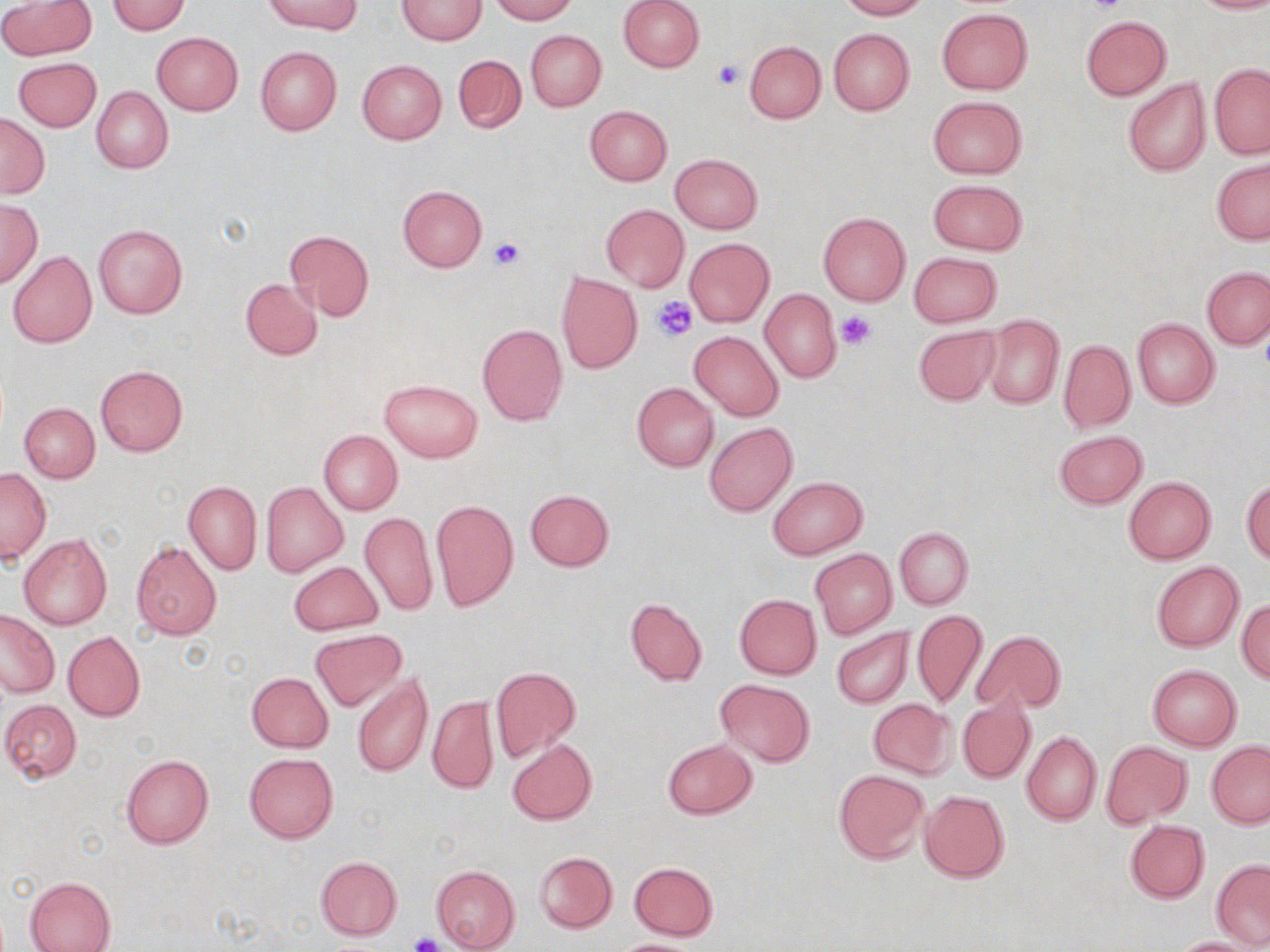

Approximate bounding boxes as (x1, y1, x2, y2) in pixels. Uninfected red blood cell locations: (266, 0, 361, 35), (489, 0, 578, 23), (617, 0, 705, 72), (837, 0, 929, 20), (1189, 0, 1270, 14), (1, 1, 95, 60), (105, 1, 191, 35), (397, 1, 486, 45), (937, 9, 1032, 94), (1080, 16, 1171, 100), (828, 28, 914, 116), (526, 30, 606, 111), (151, 31, 243, 116), (745, 40, 826, 122), (255, 46, 341, 135), (452, 54, 526, 133), (12, 57, 101, 131), (356, 59, 446, 143), (1209, 64, 1270, 159), (1123, 78, 1210, 178), (91, 87, 172, 174), (927, 95, 1026, 179), (584, 105, 672, 186), (0, 113, 50, 199), (670, 153, 762, 232), (1212, 158, 1269, 244), (927, 179, 1027, 255), (397, 184, 488, 272), (0, 199, 42, 286), (601, 204, 688, 291), (818, 212, 910, 305), (94, 224, 188, 319), (284, 227, 375, 321), (684, 237, 775, 328), (8, 251, 97, 348), (909, 252, 1002, 327), (1201, 267, 1270, 349), (555, 271, 643, 374), (240, 279, 322, 360), (760, 290, 840, 384), (984, 315, 1063, 409), (1132, 318, 1219, 408), (477, 323, 567, 425), (913, 324, 1000, 406), (689, 331, 784, 421), (1058, 339, 1135, 432), (95, 366, 188, 455), (381, 378, 482, 462), (632, 383, 718, 472), (19, 402, 99, 482), (705, 423, 796, 517), (1053, 430, 1148, 509), (319, 431, 401, 515), (0, 469, 51, 563), (768, 476, 867, 559), (1123, 476, 1216, 564), (1241, 479, 1270, 563), (184, 480, 261, 575), (262, 481, 347, 576), (525, 489, 615, 571), (430, 498, 519, 611), (360, 510, 438, 617), (895, 527, 972, 609), (19, 533, 112, 630), (131, 541, 221, 639), (810, 548, 897, 638), (289, 561, 383, 635), (1151, 561, 1243, 652), (734, 594, 821, 678), (625, 597, 707, 686), (1237, 599, 1270, 684), (0, 609, 59, 697), (911, 610, 987, 709), (831, 626, 913, 708), (311, 629, 403, 710), (972, 629, 1063, 716), (63, 630, 146, 721), (1148, 664, 1241, 750), (490, 666, 581, 762), (246, 672, 332, 752), (352, 673, 431, 778), (716, 679, 814, 766), (957, 692, 1036, 785), (427, 695, 497, 795), (2, 698, 83, 783), (867, 698, 957, 779), (1021, 731, 1101, 825), (507, 738, 597, 825), (662, 738, 757, 819), (1102, 741, 1191, 826), (1207, 741, 1270, 828), (244, 752, 338, 843), (120, 753, 214, 849), (833, 769, 930, 863), (919, 789, 1010, 883), (1124, 820, 1210, 902), (534, 851, 617, 933), (315, 856, 402, 939), (1212, 859, 1270, 947), (628, 862, 719, 940), (431, 865, 520, 952), (25, 876, 116, 952), (1170, 937, 1262, 951), (612, 938, 704, 952). Platelet locations: (1085, 0, 1129, 17), (712, 60, 745, 91), (487, 236, 526, 270), (650, 297, 698, 341), (835, 309, 879, 349), (409, 931, 446, 952). Slide-level diagnosis: no evidence of blood parasites. Image is 1270×952 pixels. May-Grünwald-Giemsa-stained preparation. One field of a larger specimen. Thin blood film. Light microscopy. 1000x magnification.